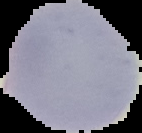

result = no Plasmodium parasites seen
image type = segmented cell region on a black background
preparation = thin blood smear
image size = 142×133 pixels